Assess the morphology of the red blood cells.
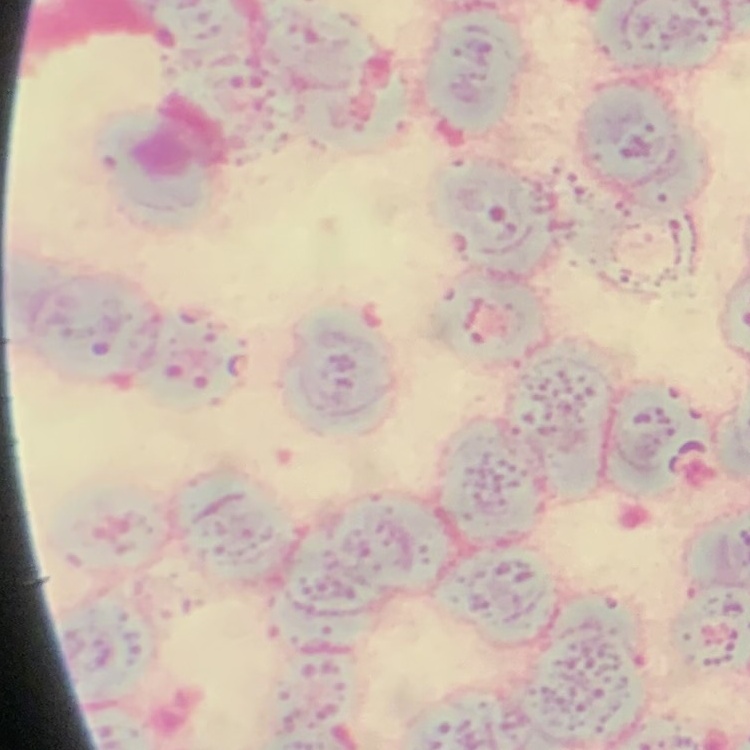

They show rouleaux formation.

Summary:
  - Preparation: thin peripheral smear
  - Image type: one tile cut from a larger photomicrograph
  - Stain: Field's or Giemsa